Identify the blood parasite species.
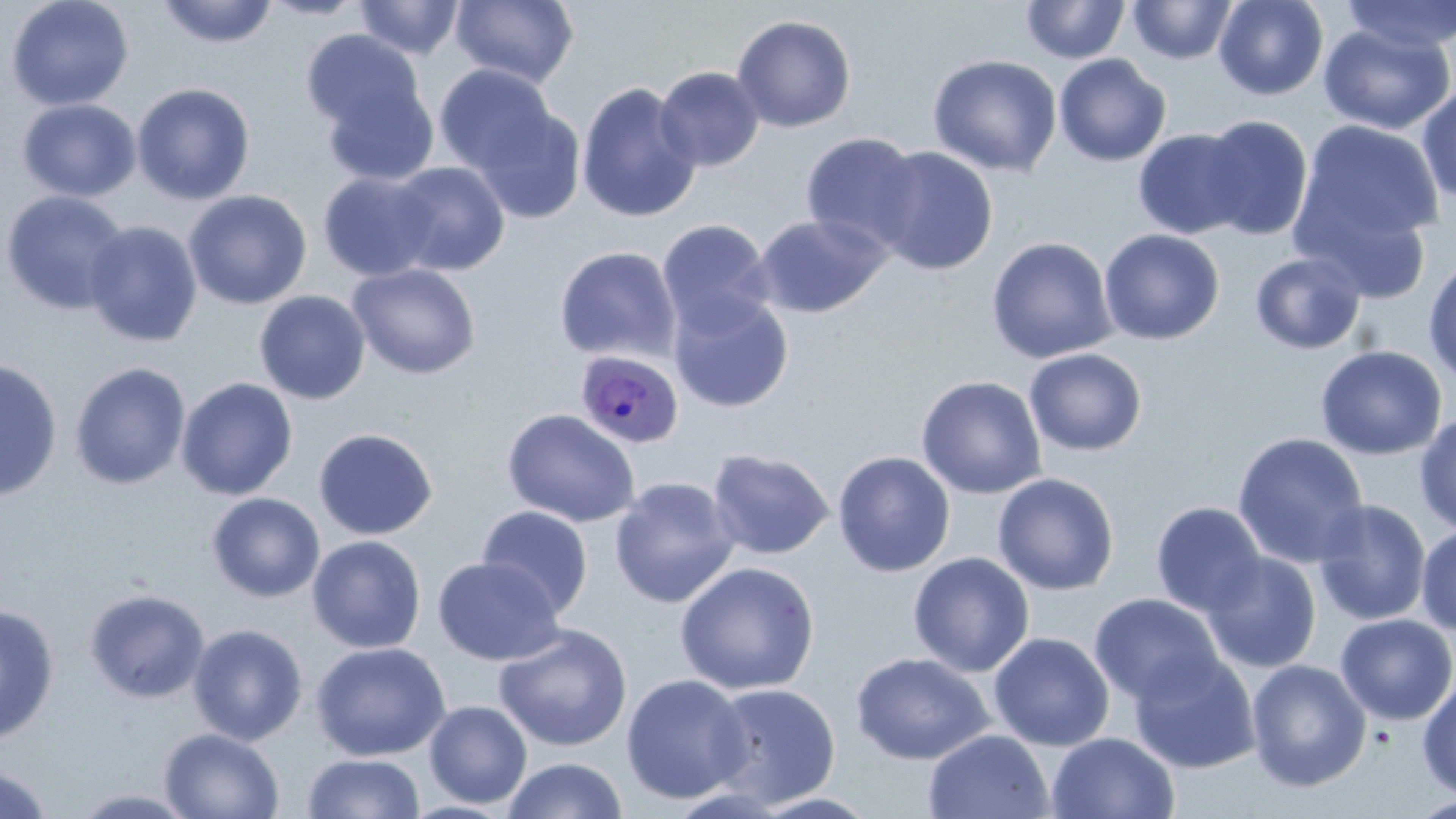

Plasmodium ovale.

magnification = 1000x
stain = May-Grünwald-Giemsa
preparation = thin blood film
modality = optical microscopy
field of view = single
uninfected red blood cell locations = approximate bounding boxes as [x1, y1, x2, y2] in pixels: [5, 0, 134, 111], [156, 0, 278, 49], [259, 0, 370, 20], [353, 0, 465, 60], [450, 0, 579, 88], [1021, 0, 1130, 64], [1128, 0, 1237, 64], [1214, 0, 1328, 101], [1339, 0, 1456, 54], [731, 14, 857, 133], [1318, 21, 1455, 135], [301, 29, 427, 141], [1054, 53, 1172, 167], [927, 54, 1063, 177], [434, 63, 558, 177], [654, 66, 765, 172], [317, 78, 441, 187], [576, 81, 702, 224], [132, 82, 256, 205], [1416, 83, 1456, 205], [17, 98, 141, 202], [471, 105, 587, 223], [1197, 114, 1314, 240], [1292, 118, 1444, 265], [1133, 128, 1253, 239], [800, 133, 924, 253], [871, 146, 998, 275], [388, 161, 511, 276], [318, 170, 439, 282], [1, 189, 130, 316], [183, 189, 312, 310], [754, 213, 890, 318], [656, 219, 776, 337], [83, 221, 203, 347], [1098, 228, 1225, 345], [986, 236, 1118, 364], [554, 246, 681, 364], [1249, 251, 1367, 355], [1423, 256, 1456, 387], [347, 262, 481, 379], [254, 290, 371, 405], [669, 290, 794, 413], [1315, 345, 1447, 461], [1024, 348, 1147, 456], [0, 358, 62, 503], [69, 362, 191, 490], [915, 375, 1047, 499], [175, 377, 298, 501], [502, 408, 640, 528], [1414, 412, 1456, 537], [313, 427, 438, 540], [1231, 432, 1369, 569], [706, 447, 834, 560], [832, 450, 956, 577], [992, 472, 1119, 596], [609, 476, 739, 608], [206, 492, 325, 602], [1313, 499, 1431, 626], [1150, 501, 1267, 617], [476, 505, 593, 618], [1415, 525, 1456, 635], [307, 535, 427, 654], [1200, 551, 1322, 673], [908, 552, 1035, 677], [432, 556, 565, 665], [674, 561, 820, 695], [85, 588, 210, 703], [1088, 593, 1225, 707], [0, 604, 59, 744], [1334, 613, 1456, 725], [187, 624, 308, 745], [493, 624, 633, 752], [988, 632, 1115, 751], [310, 642, 450, 761], [1128, 650, 1261, 774], [850, 652, 995, 764], [1246, 659, 1371, 792], [1417, 673, 1456, 802], [620, 674, 752, 804], [703, 682, 841, 809], [423, 700, 532, 808], [160, 727, 285, 819], [924, 729, 1054, 819], [1046, 731, 1180, 819], [302, 753, 425, 818], [501, 756, 629, 818], [0, 764, 55, 819], [68, 787, 202, 818], [1408, 794, 1456, 818]
Plasmodium ovale-infected red blood cell locations = approximate bounding boxes as [x1, y1, x2, y2] in pixels: [575, 350, 684, 449]
image size = 1456×819 pixels